Report the malaria status of this cell.
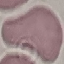

Uninfected.

preparation: thin smear
capture: smartphone through the microscope eyepiece
stain: Giemsa
image_type: cell patch, automatically extracted from a larger field of view and resized to 64 × 64 pixels